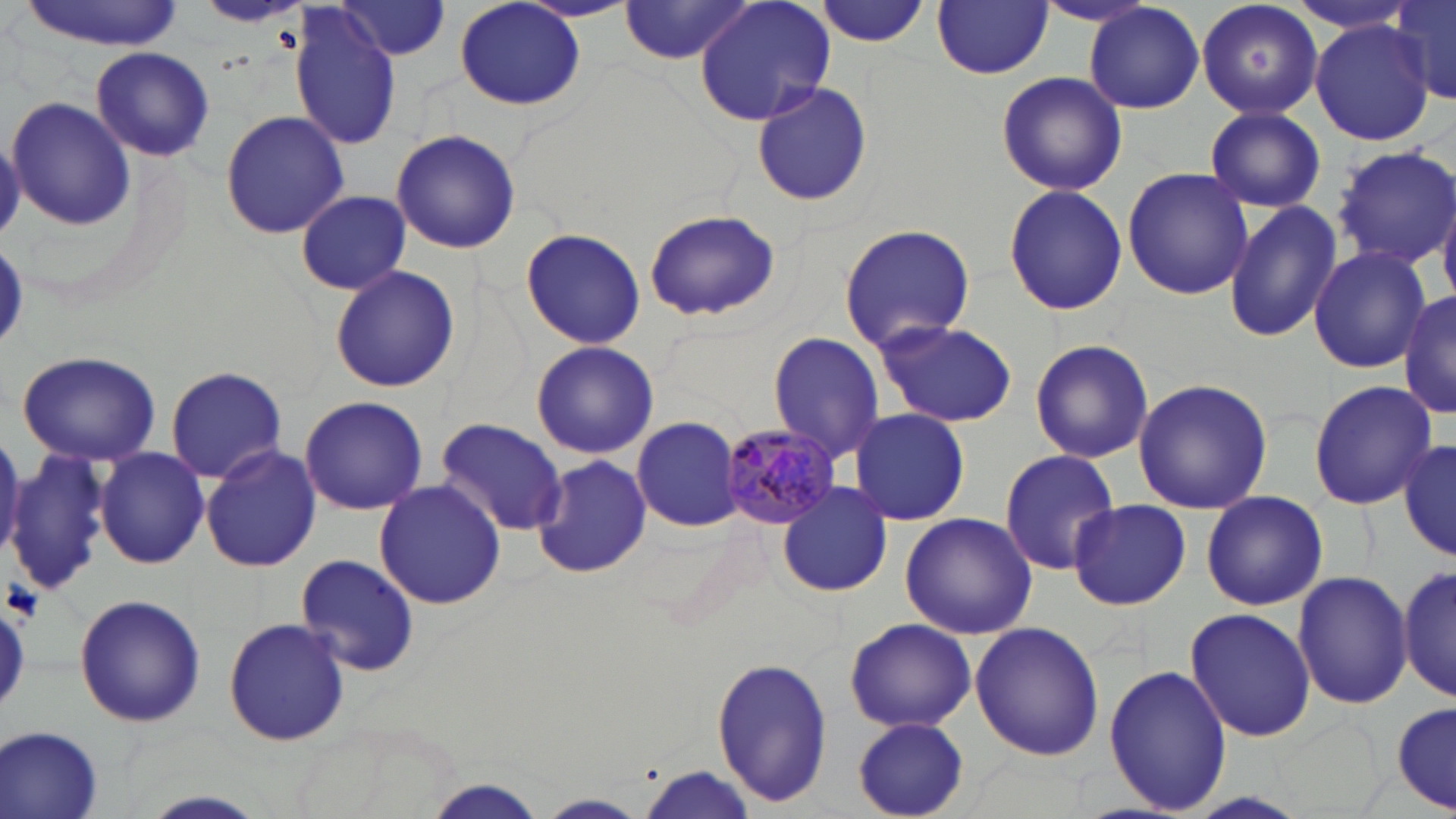
Summary:
  - Coordinate format: approximate bounding boxes as named x1/y1/x2/y2 corners in pixels
  - Uninfected red blood cell locations: (x1=336, y1=0, x2=450, y2=60), (x1=517, y1=0, x2=639, y2=23), (x1=693, y1=0, x2=836, y2=125), (x1=813, y1=0, x2=933, y2=46), (x1=1196, y1=0, x2=1323, y2=120), (x1=1388, y1=0, x2=1456, y2=101), (x1=17, y1=1, x2=188, y2=52), (x1=191, y1=1, x2=308, y2=29), (x1=455, y1=1, x2=585, y2=110), (x1=618, y1=1, x2=765, y2=67), (x1=932, y1=1, x2=1052, y2=78), (x1=1082, y1=2, x2=1205, y2=113), (x1=291, y1=7, x2=404, y2=149), (x1=1311, y1=20, x2=1436, y2=147), (x1=710, y1=32, x2=852, y2=198), (x1=91, y1=47, x2=215, y2=161), (x1=994, y1=69, x2=1128, y2=196), (x1=749, y1=81, x2=873, y2=208), (x1=7, y1=97, x2=133, y2=229), (x1=1205, y1=106, x2=1325, y2=212), (x1=219, y1=108, x2=348, y2=238), (x1=391, y1=131, x2=519, y2=253), (x1=0, y1=133, x2=23, y2=242), (x1=1331, y1=143, x2=1456, y2=270), (x1=1122, y1=167, x2=1254, y2=301), (x1=1002, y1=185, x2=1128, y2=317), (x1=296, y1=190, x2=411, y2=295), (x1=1439, y1=193, x2=1456, y2=304), (x1=1223, y1=198, x2=1340, y2=344), (x1=643, y1=208, x2=782, y2=324), (x1=837, y1=222, x2=977, y2=353), (x1=521, y1=227, x2=646, y2=350), (x1=1308, y1=245, x2=1431, y2=374), (x1=329, y1=265, x2=459, y2=394), (x1=1399, y1=285, x2=1456, y2=422), (x1=873, y1=319, x2=1017, y2=425), (x1=768, y1=331, x2=882, y2=461), (x1=1029, y1=337, x2=1154, y2=464), (x1=530, y1=340, x2=659, y2=459), (x1=15, y1=350, x2=163, y2=465), (x1=165, y1=365, x2=289, y2=484), (x1=1130, y1=379, x2=1274, y2=513), (x1=1308, y1=381, x2=1436, y2=508), (x1=298, y1=395, x2=429, y2=515), (x1=847, y1=407, x2=971, y2=527), (x1=631, y1=415, x2=741, y2=533), (x1=435, y1=418, x2=567, y2=536), (x1=0, y1=426, x2=23, y2=562), (x1=1399, y1=436, x2=1455, y2=565), (x1=201, y1=445, x2=323, y2=572), (x1=95, y1=448, x2=211, y2=569), (x1=6, y1=449, x2=114, y2=595), (x1=998, y1=450, x2=1120, y2=576), (x1=530, y1=455, x2=654, y2=578), (x1=374, y1=480, x2=508, y2=610), (x1=779, y1=484, x2=892, y2=597), (x1=1200, y1=490, x2=1327, y2=611), (x1=1068, y1=497, x2=1193, y2=610), (x1=899, y1=512, x2=1037, y2=640), (x1=296, y1=552, x2=421, y2=678), (x1=1401, y1=566, x2=1456, y2=701), (x1=1293, y1=571, x2=1414, y2=708), (x1=74, y1=593, x2=207, y2=727), (x1=1184, y1=607, x2=1316, y2=742), (x1=223, y1=615, x2=350, y2=747), (x1=844, y1=617, x2=976, y2=732), (x1=969, y1=621, x2=1104, y2=762), (x1=711, y1=657, x2=833, y2=807), (x1=1103, y1=661, x2=1233, y2=815), (x1=1390, y1=698, x2=1454, y2=814), (x1=852, y1=716, x2=969, y2=818), (x1=1, y1=726, x2=104, y2=818), (x1=638, y1=765, x2=758, y2=819), (x1=421, y1=778, x2=550, y2=818), (x1=144, y1=791, x2=272, y2=817), (x1=535, y1=795, x2=650, y2=819)
  - Plasmodium malariae-infected red blood cell locations: (x1=718, y1=422, x2=846, y2=529)
  - Slide-level diagnosis: Plasmodium malariae
  - Stain: May-Grünwald-Giemsa
  - Field of view: one of a larger specimen
  - Modality: optical microscopy
  - Preparation: thin blood film
  - Image size: 1456×819 pixels
  - Magnification: 1000x